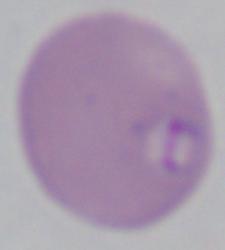

modality = photomicrograph
identification = Babesia
magnification = 1000x